State which cell type is depicted.
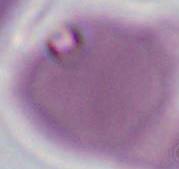
An erythrocyte.

1000x magnification. Photomicrograph.